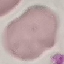
Summary:
  - Malaria status: uninfected
  - Preparation: thin blood smear
  - Stain: Giemsa
  - Capture: smartphone through the microscope eyepiece
  - Image type: cell patch, automatically extracted from a larger field of view and resized to 64 × 64 pixels